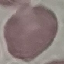

{
  "result": "no malaria parasites seen",
  "stain": "Giemsa",
  "image_type": "automatically extracted cell patch, resized to 64 × 64 pixels",
  "capture": "smartphone camera at the microscope eyepiece",
  "preparation": "thin blood film"
}